State the blood parasite species.
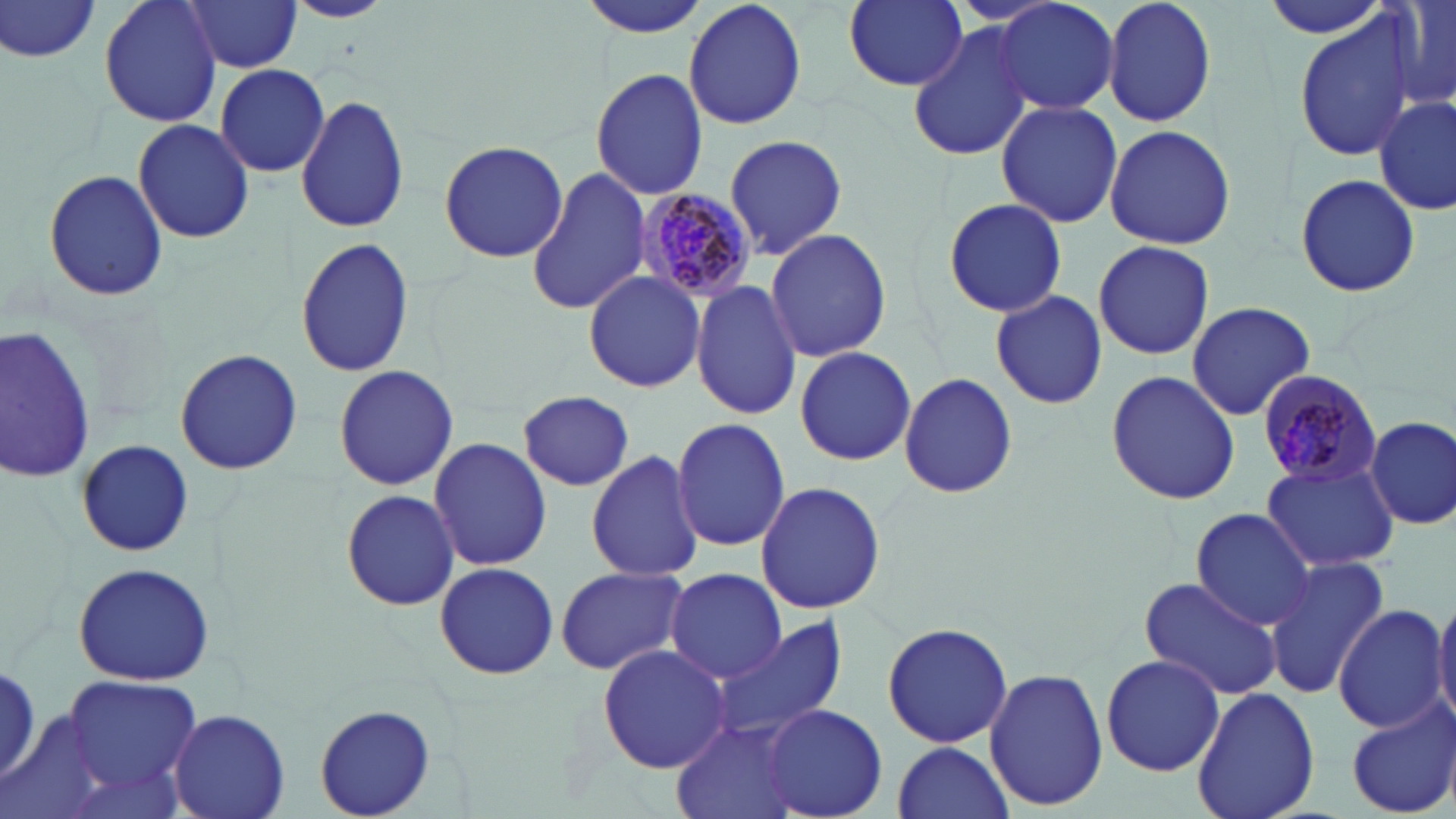

Plasmodium malariae.

magnification: 1000x
image_size: 1456×819 pixels
stain: May-Grünwald-Giemsa
preparation: thin blood film
uninfected_red_blood_cell_locations: 'approximate bounding boxes as (x1,y1)-(x2,y2) corner pairs in pixels: (0,0)-(105,64), (99,0)-(224,129), (684,0)-(808,134), (839,0)-(968,93), (992,0)-(1119,115), (1102,0)-(1216,129), (1260,0)-(1397,40), (1385,0)-(1456,116), (180,1)-(304,74), (279,1)-(397,25), (577,1)-(712,40), (1294,7)-(1421,163), (907,21)-(1035,163), (216,64)-(330,176), (589,66)-(710,199), (297,94)-(410,234), (1374,98)-(1455,213), (996,100)-(1125,229), (132,119)-(256,245), (1103,124)-(1238,249), (722,133)-(848,261), (438,139)-(569,264), (525,166)-(652,318), (43,169)-(168,302), (1293,172)-(1422,299), (940,197)-(1069,319), (765,228)-(892,361), (296,237)-(414,379), (1092,241)-(1214,359), (583,269)-(705,392), (692,280)-(803,422), (990,290)-(1107,410), (1186,300)-(1316,421), (0,323)-(96,484), (794,346)-(916,466), (175,349)-(302,475), (332,363)-(462,490), (1104,370)-(1242,505), (898,371)-(1020,500), (518,390)-(634,490), (1364,415)-(1456,530), (670,416)-(791,550), (540,426)-(670,548), (429,436)-(552,573), (76,438)-(192,559), (587,450)-(703,581), (1262,459)-(1398,572), (755,480)-(885,614), (337,492)-(462,613), (1190,508)-(1318,630), (1263,554)-(1391,697), (433,559)-(559,680), (72,562)-(217,684), (555,565)-(688,676), (663,568)-(785,682), (1138,574)-(1282,702), (1432,591)-(1456,725), (1334,605)-(1449,732), (706,613)-(849,747), (882,621)-(1012,750), (598,643)-(733,774), (1101,652)-(1225,776), (1,660)-(43,788), (985,665)-(1108,811), (64,678)-(205,789), (1192,686)-(1323,819), (1346,700)-(1456,817), (312,703)-(439,818), (763,703)-(887,817), (168,708)-(289,819), (671,720)-(806,819), (892,741)-(1014,819)'
modality: light microscopy
plasmodium_malariae_infected_red_blood_cell_locations: 'approximate bounding boxes as (x1,y1)-(x2,y2) corner pairs in pixels: (633,188)-(757,302), (1254,369)-(1383,488)'
field_of_view: one of a larger specimen